Evaluate for malaria.
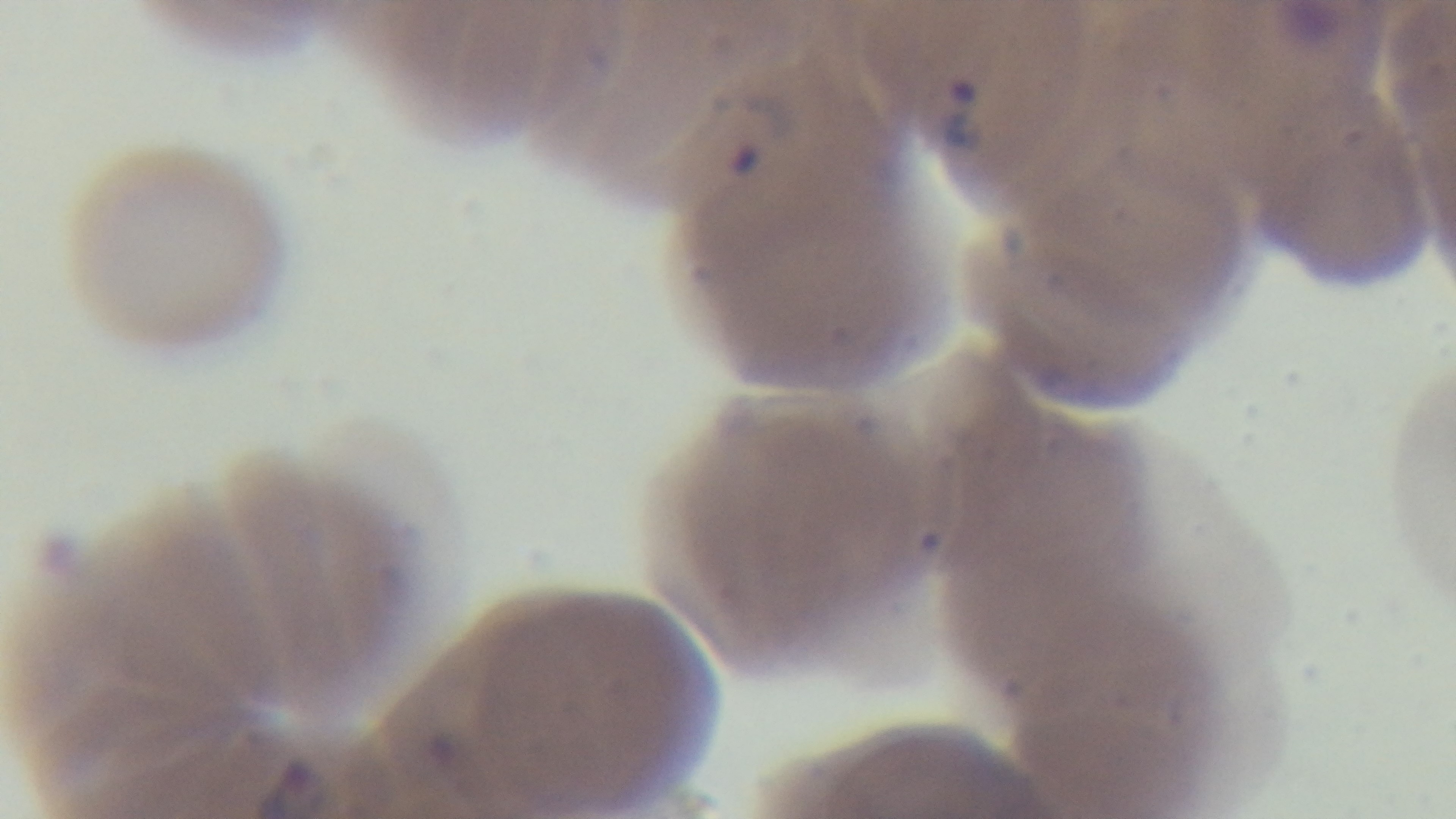

Positive.

Summary:
  - Capture: mounted 4K digital camera
  - Modality: light microscopy
  - Field of view: single
  - Objective: 100x oil immersion
  - Preparation: thin smear
  - Stain: Giemsa